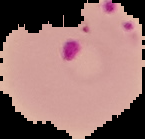
Summary:
  - Preparation: thin blood smear
  - Malaria status: parasitized
  - Image type: segmented cell region with the area outside set to black
  - Image size: 145×139 pixels